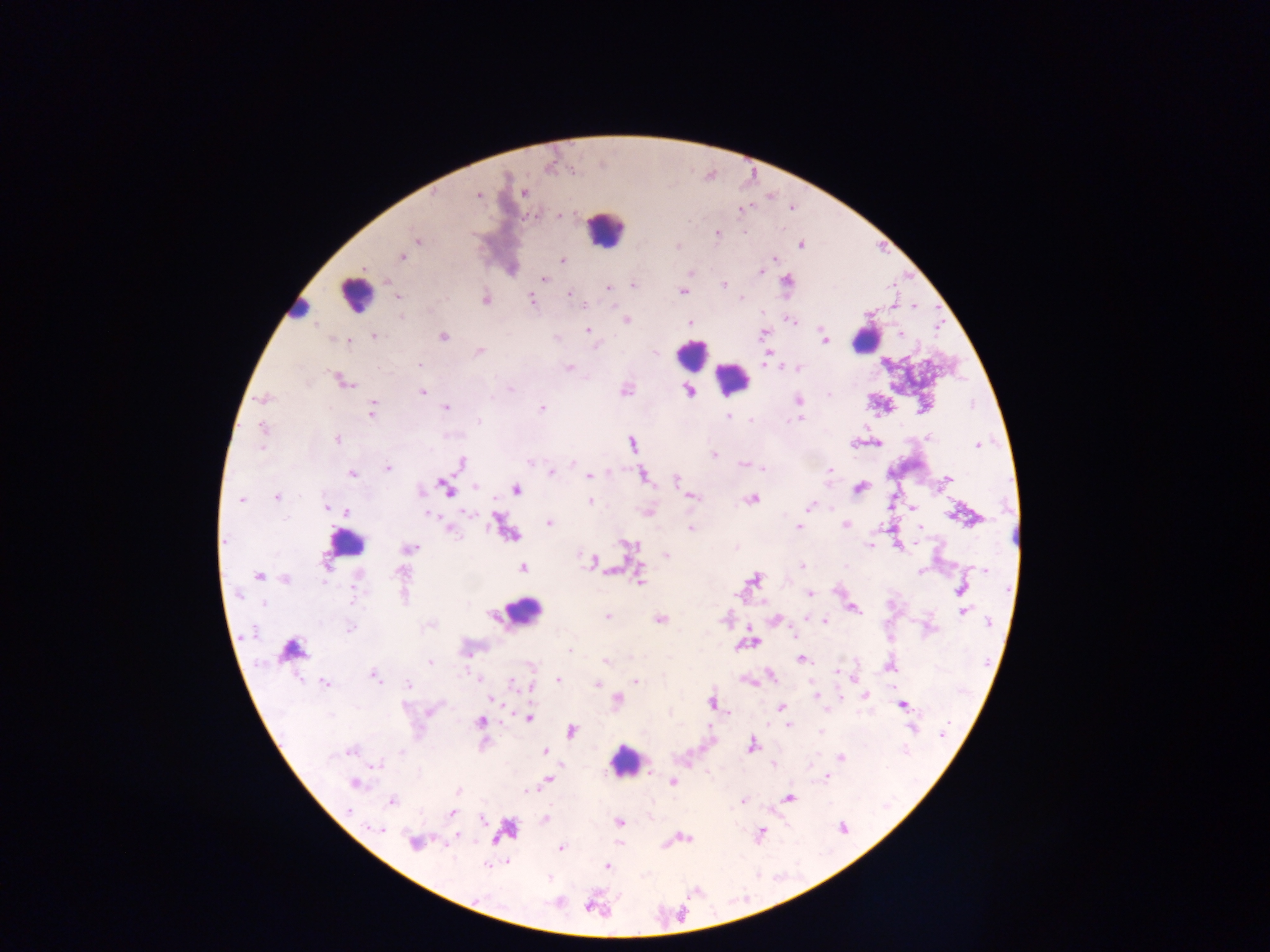
Approximate centers as {x, y} in pixels. Plasmodium parasite locations: {523, 193}, {478, 196}, {741, 209}, {560, 215}, {717, 232}, {744, 233}, {417, 241}, {801, 245}, {677, 246}, {402, 256}, {774, 258}, {562, 260}, {760, 272}, {543, 278}, {786, 280}, {723, 284}, {633, 285}, {608, 287}, {683, 291}, {569, 294}, {398, 297}, {742, 298}, {532, 299}, {486, 300}, {915, 306}, {790, 319}, {625, 320}, {690, 323}, {588, 330}, {763, 334}, {900, 334}, {374, 336}, {443, 336}, {825, 340}, {349, 341}, {480, 352}, {655, 353}, {419, 365}, {569, 367}, {798, 368}, {343, 382}, {511, 389}, {625, 389}, {422, 392}, {689, 392}, {829, 394}, {491, 398}, {264, 399}, {798, 400}, {446, 408}, {542, 408}, {372, 411}, {728, 415}, {750, 419}, {798, 419}, {479, 421}, {263, 428}, {929, 437}, {337, 439}, {633, 444}, {877, 444}, {977, 445}, {261, 447}, {714, 454}, {530, 462}, {461, 463}, {573, 463}, {743, 464}, {388, 468}, {763, 469}, {830, 469}, {551, 472}, {352, 474}, {589, 476}, {643, 476}, {948, 478}, {676, 480}, {476, 486}, {859, 488}, {446, 489}, {516, 489}, {421, 491}, {690, 496}, {277, 497}, {751, 499}, {240, 500}, {590, 501}, {809, 506}, {326, 508}, {913, 508}, {347, 511}, {468, 513}, {429, 515}, {286, 518}, {549, 523}, {845, 524}, {499, 525}, {798, 527}, {920, 527}, {690, 528}, {450, 529}, {226, 541}, {629, 545}, {870, 545}, {411, 548}, {666, 555}, {592, 561}, {802, 566}, {523, 568}, {985, 569}, {401, 571}, {921, 572}, {259, 576}, {285, 579}, {754, 579}, {639, 580}, {357, 588}, {961, 590}, {810, 594}, {264, 604}, {854, 609}, {964, 612}, {606, 617}, {660, 620}, {825, 621}, {989, 622}, {350, 628}, {291, 650}, {570, 651}, {802, 660}, {605, 662}, {430, 663}, {890, 666}, {836, 672}, {771, 675}, {374, 676}, {478, 678}, {558, 680}, {636, 681}, {325, 683}, {513, 683}, {597, 684}, {409, 685}, {816, 696}, {865, 696}, {492, 700}, {618, 700}, {712, 703}, {902, 706}, {404, 707}, {782, 707}, {431, 711}, {528, 718}, {480, 722}, {789, 725}, {571, 731}, {821, 731}, {943, 733}, {752, 745}, {350, 751}, {401, 751}, {545, 752}, {840, 758}, {377, 765}, {774, 765}, {649, 773}, {828, 777}, {549, 779}, {673, 782}, {354, 783}, {458, 791}, {528, 791}, {790, 798}, {392, 801}, {742, 801}, {349, 811}, {451, 813}, {545, 818}, {483, 819}, {619, 822}, {379, 829}, {843, 829}, {761, 834}, {457, 836}, {415, 842}, {560, 847}, {487, 865}, {606, 866}, {588, 907}. Leukocyte locations: {605, 229}, {355, 295}, {298, 308}, {865, 340}, {691, 354}, {733, 378}, {346, 543}, {522, 612}, {623, 760}. Thick blood film. Photographed through a microscope with a mobile-phone camera. One field of view. Image is 1270×952 pixels. Collected in Ghana.